State the preparation type.
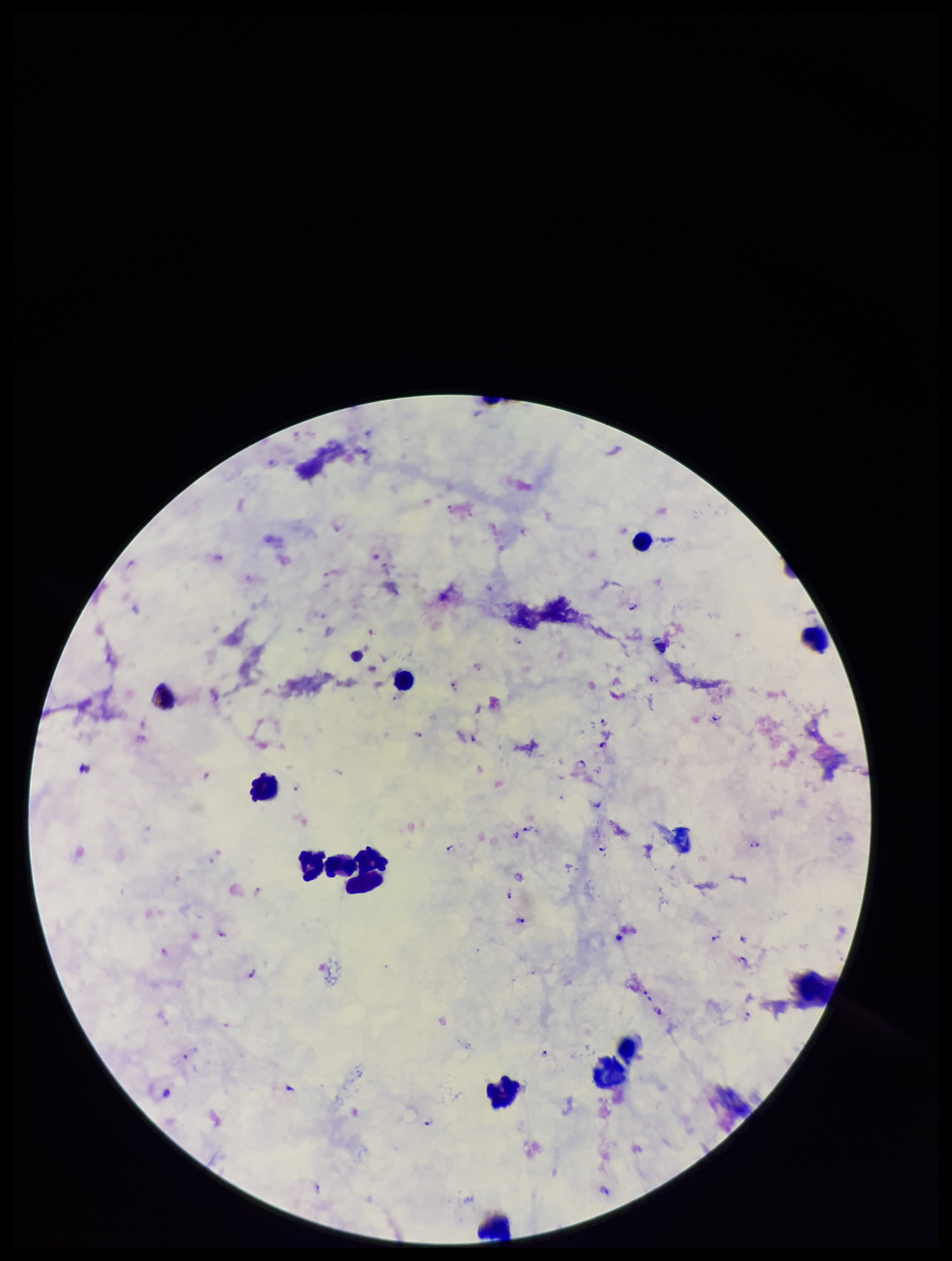
Thick.

{
  "image_size": "952×1261 pixels",
  "plasmodium_parasites": "seen",
  "patient_malaria_status": "infected",
  "parasite_count": 29,
  "species_reported_for_this_patient": "Plasmodium falciparum",
  "capture": "smartphone photograph through the microscope eyepiece",
  "leukocyte_count": 12,
  "stain": "Giemsa",
  "field_of_view": "one from this slide"
}